Identify the blood parasite species.
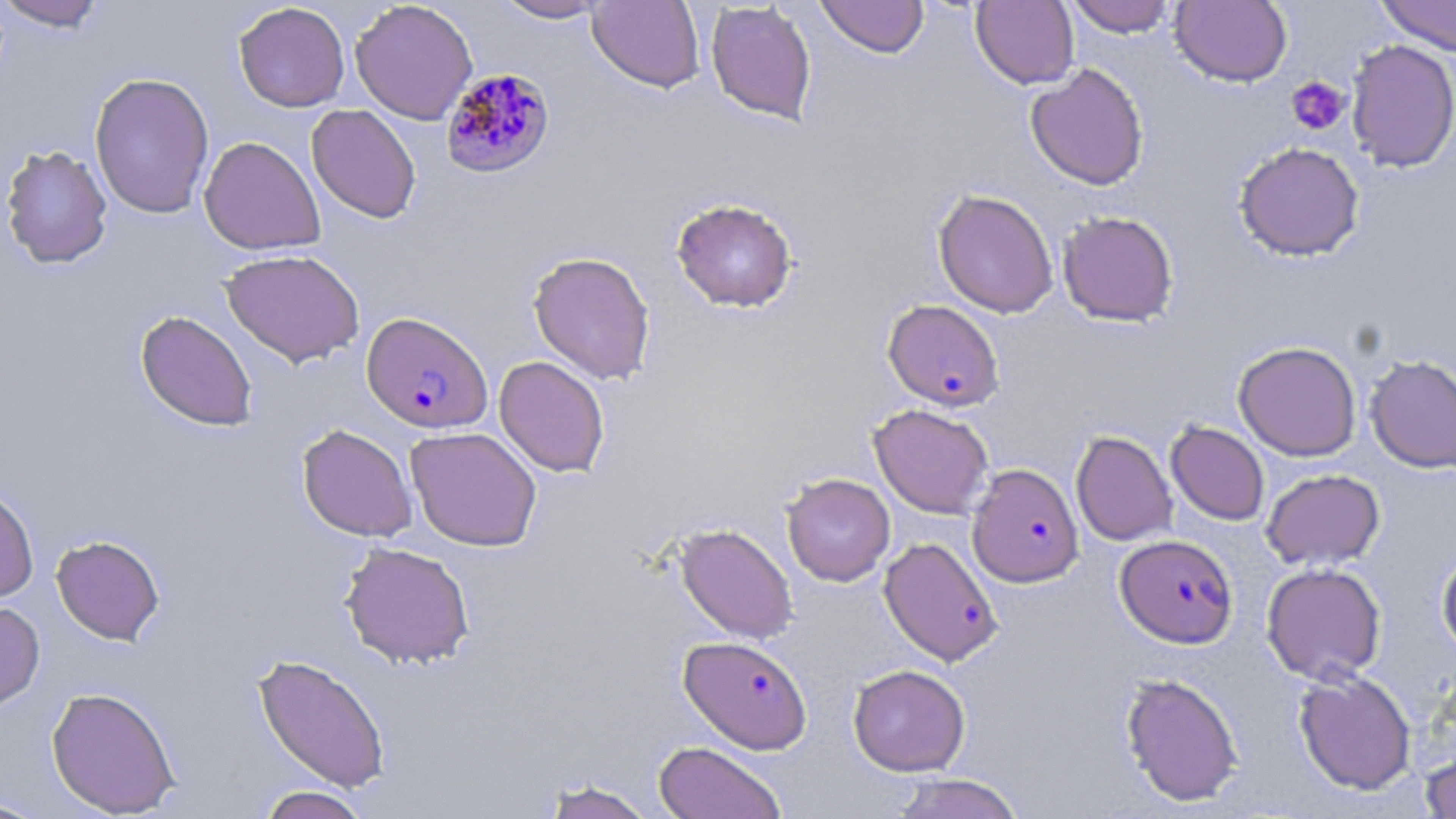
Plasmodium falciparum.

Approximate bounding boxes as named x1/y1/x2/y2 corners in pixels. Plasmodium falciparum-infected red blood cell locations (subset): (x1=440, y1=67, x2=556, y2=180), (x1=362, y1=311, x2=493, y2=433), (x1=967, y1=463, x2=1083, y2=587), (x1=1115, y1=534, x2=1238, y2=648), (x1=879, y1=536, x2=1004, y2=666), (x1=678, y1=635, x2=813, y2=754). Platelet locations: (x1=1286, y1=76, x2=1350, y2=135). Uninfected red blood cell locations (subset): (x1=0, y1=0, x2=109, y2=31), (x1=350, y1=0, x2=477, y2=124), (x1=491, y1=0, x2=610, y2=23), (x1=816, y1=0, x2=929, y2=58), (x1=1065, y1=0, x2=1179, y2=37), (x1=1170, y1=0, x2=1292, y2=87), (x1=1376, y1=0, x2=1456, y2=56), (x1=587, y1=1, x2=819, y2=105), (x1=587, y1=1, x2=705, y2=93), (x1=705, y1=1, x2=818, y2=126), (x1=971, y1=1, x2=1079, y2=89), (x1=233, y1=2, x2=350, y2=112), (x1=1346, y1=39, x2=1456, y2=173), (x1=1025, y1=63, x2=1150, y2=190), (x1=89, y1=72, x2=215, y2=218), (x1=306, y1=104, x2=422, y2=224), (x1=199, y1=136, x2=325, y2=255), (x1=1234, y1=142, x2=1365, y2=262), (x1=1, y1=144, x2=113, y2=269), (x1=932, y1=189, x2=1059, y2=318), (x1=671, y1=198, x2=798, y2=313), (x1=1057, y1=210, x2=1179, y2=327), (x1=221, y1=249, x2=365, y2=367), (x1=528, y1=250, x2=656, y2=385), (x1=135, y1=310, x2=257, y2=431), (x1=1233, y1=340, x2=1362, y2=461), (x1=1364, y1=354, x2=1456, y2=473), (x1=494, y1=355, x2=610, y2=477), (x1=869, y1=403, x2=994, y2=519), (x1=1166, y1=421, x2=1269, y2=526), (x1=297, y1=424, x2=417, y2=542), (x1=405, y1=427, x2=542, y2=552), (x1=1071, y1=430, x2=1177, y2=546), (x1=1261, y1=468, x2=1385, y2=569), (x1=781, y1=473, x2=895, y2=586), (x1=0, y1=486, x2=39, y2=603), (x1=674, y1=523, x2=798, y2=644), (x1=51, y1=535, x2=165, y2=645), (x1=338, y1=541, x2=476, y2=669), (x1=1436, y1=545, x2=1456, y2=656), (x1=1261, y1=562, x2=1386, y2=685), (x1=0, y1=601, x2=45, y2=711), (x1=253, y1=653, x2=391, y2=792), (x1=848, y1=664, x2=970, y2=776), (x1=1293, y1=669, x2=1416, y2=795), (x1=1119, y1=672, x2=1244, y2=807), (x1=46, y1=686, x2=181, y2=817), (x1=653, y1=741, x2=787, y2=819), (x1=1421, y1=742, x2=1455, y2=818), (x1=890, y1=773, x2=1025, y2=819), (x1=539, y1=777, x2=658, y2=819), (x1=255, y1=785, x2=371, y2=819), (x1=0, y1=796, x2=51, y2=818). 1000x magnification. Image is 1456×819 pixels. Thin blood smear. May-Grünwald-Giemsa-stained preparation. Optical microscopy. One field of a larger specimen.